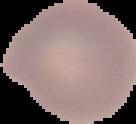

result = no Plasmodium parasites detected
image size = 136×124 pixels
preparation = thin blood film
image type = cell region segmented out of the field of view; surrounding area masked to black